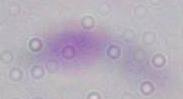
Summary:
  - Magnification: 1000x
  - Modality: micrograph
  - Identification: Toxoplasma gondii